Report the malaria status of this cell.
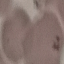
Uninfected.

Summary:
  - Stain: Giemsa
  - Preparation: thin smear
  - Capture: smartphone camera at the microscope eyepiece
  - Image type: automatically extracted cell patch, resized to 64 × 64 pixels